Outline each Plasmodium vivax-infected red blood cell.
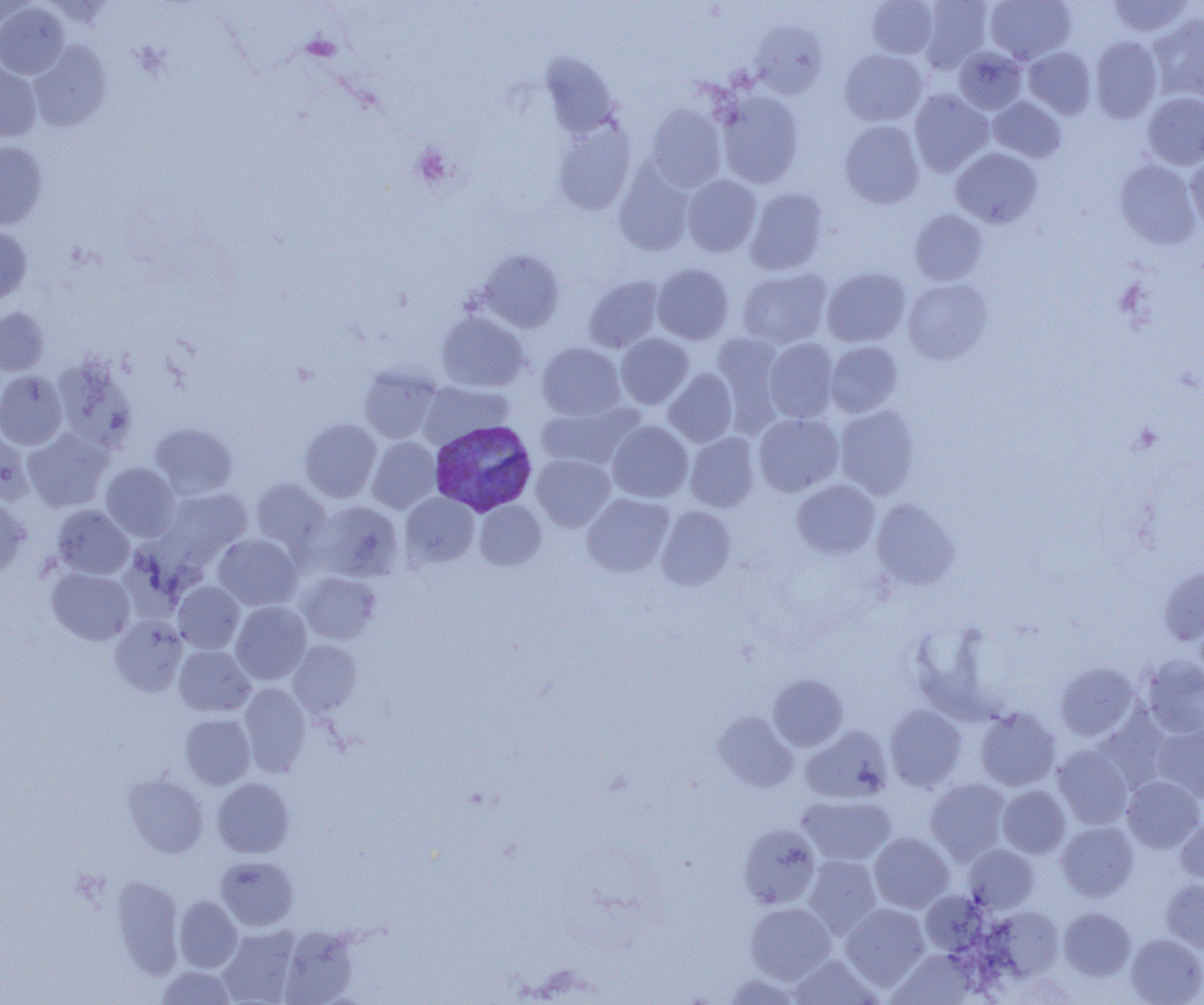

Approximate bounding boxes as named x1/y1/x2/y2 corners in pixels.
Plasmodium vivax-infected red blood cells: (x1=429, y1=420, x2=537, y2=516).

slide_level_diagnosis: Plasmodium vivax
uninfected_red_blood_cell_locations: 'approximate bounding boxes as named x1/y1/x2/y2 corners in pixels: (x1=867, y1=0, x2=938, y2=58), (x1=918, y1=0, x2=993, y2=73), (x1=985, y1=0, x2=1076, y2=64), (x1=1107, y1=0, x2=1195, y2=38), (x1=0, y1=1, x2=38, y2=31), (x1=0, y1=2, x2=69, y2=79), (x1=1148, y1=14, x2=1204, y2=102), (x1=750, y1=19, x2=828, y2=98), (x1=1090, y1=36, x2=1163, y2=123), (x1=28, y1=40, x2=111, y2=131), (x1=954, y1=46, x2=1027, y2=115), (x1=1024, y1=47, x2=1096, y2=119), (x1=839, y1=49, x2=927, y2=126), (x1=540, y1=53, x2=621, y2=139), (x1=0, y1=60, x2=41, y2=143), (x1=909, y1=89, x2=994, y2=176), (x1=717, y1=91, x2=804, y2=188), (x1=1142, y1=91, x2=1204, y2=169), (x1=988, y1=96, x2=1066, y2=162), (x1=646, y1=103, x2=727, y2=191), (x1=839, y1=121, x2=924, y2=208), (x1=552, y1=122, x2=635, y2=215), (x1=0, y1=141, x2=47, y2=230), (x1=951, y1=148, x2=1042, y2=228), (x1=1185, y1=154, x2=1204, y2=234), (x1=1114, y1=160, x2=1200, y2=248), (x1=614, y1=165, x2=695, y2=256), (x1=681, y1=174, x2=761, y2=257), (x1=745, y1=188, x2=828, y2=274), (x1=909, y1=209, x2=988, y2=285), (x1=0, y1=225, x2=32, y2=304), (x1=477, y1=249, x2=564, y2=332), (x1=652, y1=263, x2=734, y2=345), (x1=737, y1=268, x2=832, y2=349), (x1=822, y1=268, x2=911, y2=347), (x1=583, y1=275, x2=663, y2=353), (x1=902, y1=278, x2=993, y2=364), (x1=0, y1=307, x2=49, y2=375), (x1=436, y1=311, x2=529, y2=392), (x1=711, y1=331, x2=786, y2=434), (x1=616, y1=333, x2=694, y2=409), (x1=764, y1=338, x2=839, y2=422), (x1=824, y1=341, x2=903, y2=417), (x1=537, y1=343, x2=625, y2=420), (x1=52, y1=357, x2=138, y2=451), (x1=359, y1=367, x2=442, y2=443), (x1=663, y1=368, x2=738, y2=447), (x1=0, y1=370, x2=67, y2=449), (x1=417, y1=381, x2=513, y2=449), (x1=536, y1=400, x2=644, y2=470), (x1=835, y1=405, x2=920, y2=500), (x1=753, y1=413, x2=844, y2=496), (x1=300, y1=418, x2=381, y2=502), (x1=607, y1=420, x2=693, y2=502), (x1=150, y1=423, x2=238, y2=499), (x1=0, y1=426, x2=33, y2=505), (x1=22, y1=427, x2=112, y2=512), (x1=685, y1=432, x2=760, y2=512), (x1=368, y1=437, x2=441, y2=513), (x1=531, y1=454, x2=615, y2=531), (x1=100, y1=462, x2=180, y2=541), (x1=250, y1=479, x2=331, y2=553), (x1=792, y1=480, x2=879, y2=558), (x1=161, y1=488, x2=252, y2=562), (x1=400, y1=492, x2=479, y2=568), (x1=582, y1=493, x2=674, y2=577), (x1=0, y1=495, x2=29, y2=580), (x1=870, y1=498, x2=960, y2=590), (x1=474, y1=500, x2=546, y2=570), (x1=312, y1=501, x2=404, y2=581), (x1=52, y1=505, x2=134, y2=579), (x1=656, y1=506, x2=736, y2=591), (x1=213, y1=534, x2=301, y2=610), (x1=1159, y1=566, x2=1204, y2=645), (x1=47, y1=567, x2=135, y2=644), (x1=297, y1=572, x2=381, y2=644), (x1=173, y1=581, x2=244, y2=653), (x1=231, y1=601, x2=311, y2=684), (x1=110, y1=616, x2=188, y2=696), (x1=288, y1=640, x2=362, y2=716), (x1=174, y1=645, x2=255, y2=717), (x1=1141, y1=655, x2=1204, y2=739), (x1=1055, y1=662, x2=1139, y2=741), (x1=768, y1=674, x2=848, y2=751), (x1=239, y1=683, x2=311, y2=776), (x1=885, y1=705, x2=967, y2=791), (x1=975, y1=707, x2=1060, y2=791), (x1=1095, y1=710, x2=1173, y2=794), (x1=713, y1=711, x2=798, y2=792), (x1=180, y1=714, x2=255, y2=788), (x1=1152, y1=723, x2=1204, y2=802), (x1=801, y1=725, x2=893, y2=803), (x1=1053, y1=745, x2=1133, y2=829), (x1=123, y1=775, x2=208, y2=857), (x1=1122, y1=776, x2=1203, y2=852), (x1=212, y1=778, x2=293, y2=857), (x1=925, y1=778, x2=1010, y2=865), (x1=997, y1=785, x2=1071, y2=857), (x1=797, y1=794, x2=895, y2=866), (x1=1176, y1=814, x2=1204, y2=886), (x1=1056, y1=823, x2=1138, y2=901), (x1=738, y1=824, x2=820, y2=909), (x1=869, y1=833, x2=954, y2=912), (x1=964, y1=844, x2=1039, y2=913), (x1=216, y1=856, x2=298, y2=930), (x1=804, y1=856, x2=881, y2=940), (x1=111, y1=876, x2=184, y2=977), (x1=1161, y1=878, x2=1204, y2=952), (x1=920, y1=890, x2=988, y2=955), (x1=174, y1=895, x2=242, y2=972), (x1=745, y1=902, x2=836, y2=983), (x1=840, y1=903, x2=930, y2=990), (x1=986, y1=907, x2=1064, y2=982), (x1=1059, y1=907, x2=1135, y2=980), (x1=216, y1=926, x2=301, y2=1005), (x1=278, y1=926, x2=360, y2=1005), (x1=1125, y1=933, x2=1204, y2=1005), (x1=890, y1=949, x2=977, y2=1005), (x1=788, y1=954, x2=881, y2=1004), (x1=156, y1=966, x2=237, y2=1004), (x1=721, y1=974, x2=803, y2=1005)'
field_of_view: single
preparation: thin blood smear
platelet_locations: 'approximate bounding boxes as named x1/y1/x2/y2 corners in pixels: (x1=411, y1=145, x2=454, y2=189)'
magnification: 1000x
modality: light microscopy
image_size: 1204×1005 pixels